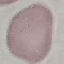

Summary:
  - Malaria status: uninfected
  - Preparation: thin smear
  - Image type: cell patch, automatically extracted from a larger field of view and resized to 64 × 64 pixels
  - Stain: Giemsa
  - Capture: smartphone through the microscope eyepiece